Name the cell type shown.
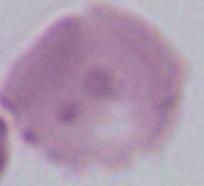
This is an erythrocyte.

Photomicrograph. 1000x magnification.